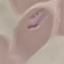

{
  "malaria_status": "parasitized",
  "stain": "Giemsa",
  "image_type": "automatically extracted cell patch, resized to 64 × 64 pixels",
  "capture": "smartphone camera at the microscope eyepiece",
  "preparation": "thin blood film"
}